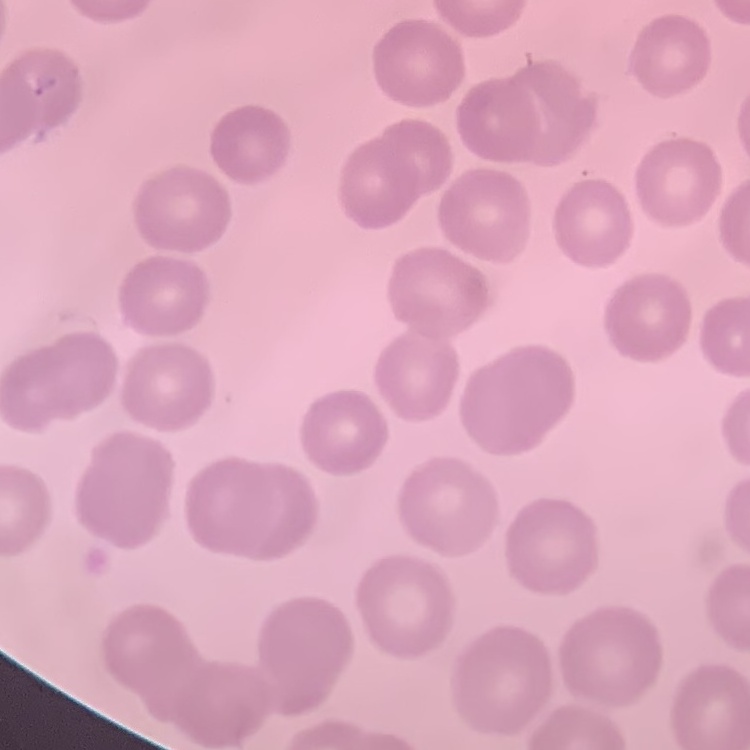

{
  "red_blood_cell_morphology": "no rouleaux formation",
  "image_type": "one tile cut from a larger photomicrograph",
  "stain": "Field's or Giemsa",
  "preparation": "thin blood film"
}